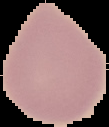

image size = 109×127 pixels
preparation = thin blood film
result = negative for malaria parasites
image type = cell region segmented out of the field of view; surrounding area masked to black